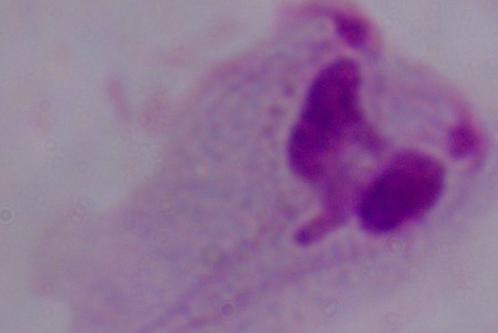

{
  "identification": "trichomonad",
  "magnification": "1000x",
  "modality": "photomicrograph"
}